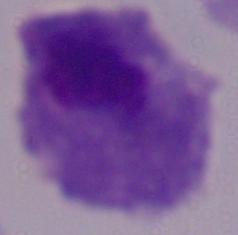

Summary:
  - Modality: photomicrograph
  - Magnification: 1000x
  - Identification: trichomonad